Assess this cell for malaria.
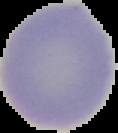

Uninfected.

image_size: 118×133 pixels
preparation: thin blood film
image_type: segmented cell region on a black background